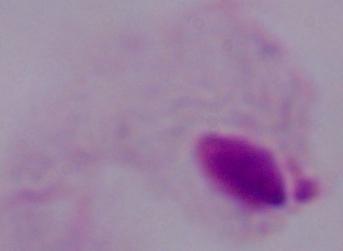
modality = micrograph
magnification = 1000x
identification = trichomonad